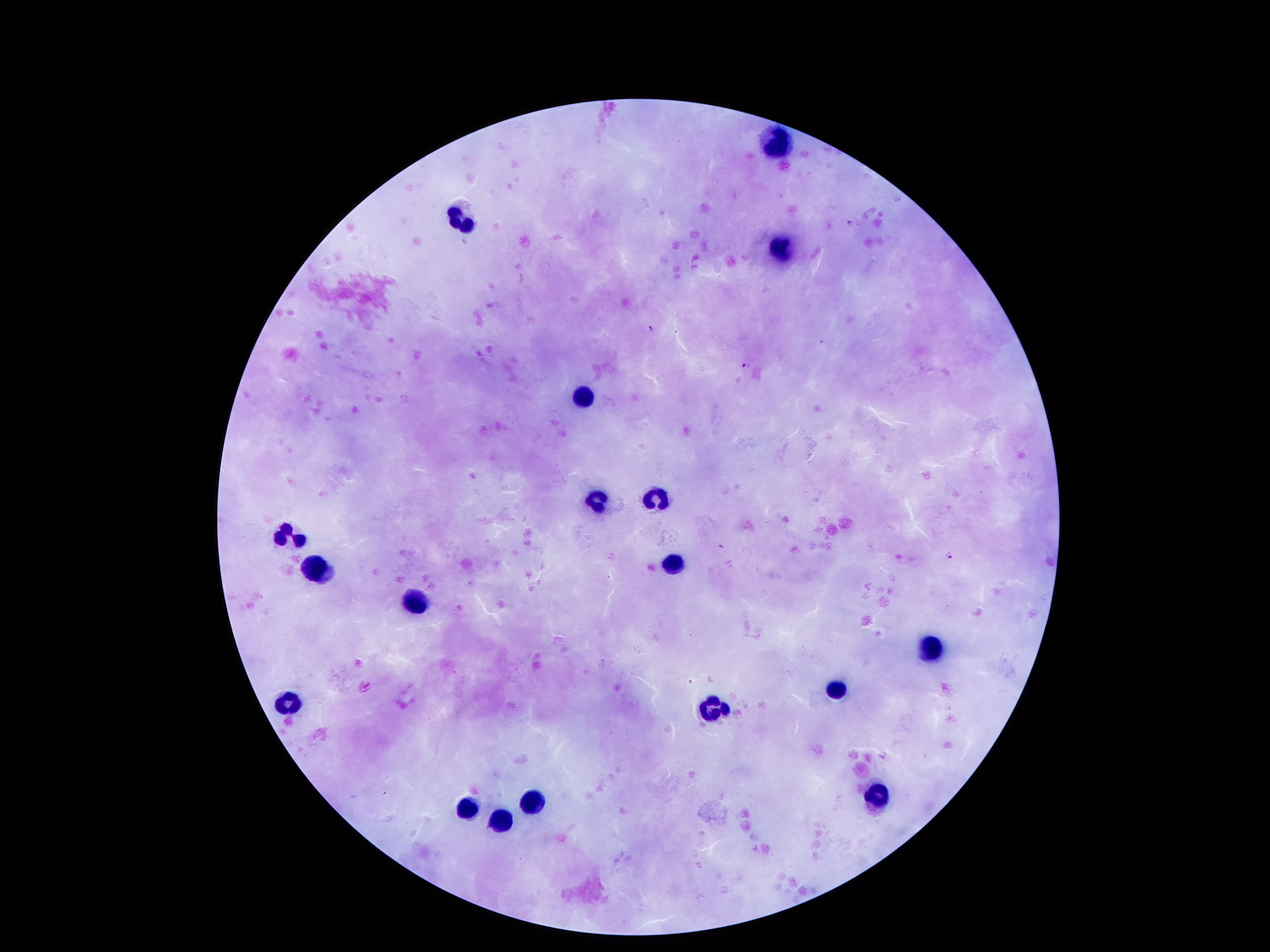

Approximate centers as (x, y) in pixels.
Summary:
  - Malaria parasite locations: (850, 222), (650, 329), (746, 366), (721, 546), (950, 554)
  - Leukocyte locations: (775, 146), (458, 222), (783, 248), (586, 398), (654, 497), (600, 503), (293, 536), (671, 564), (316, 570), (419, 601), (927, 648), (838, 690), (288, 704), (710, 708), (874, 795), (535, 796), (468, 809), (503, 820)
  - Magnification: 100x
  - Stain: Giemsa
  - Image size: 1270×952 pixels
  - Field of view: single
  - Capture: smartphone camera through the microscope eyepiece
  - Patient malaria status: infected with Plasmodium falciparum
  - Preparation: thick blood film